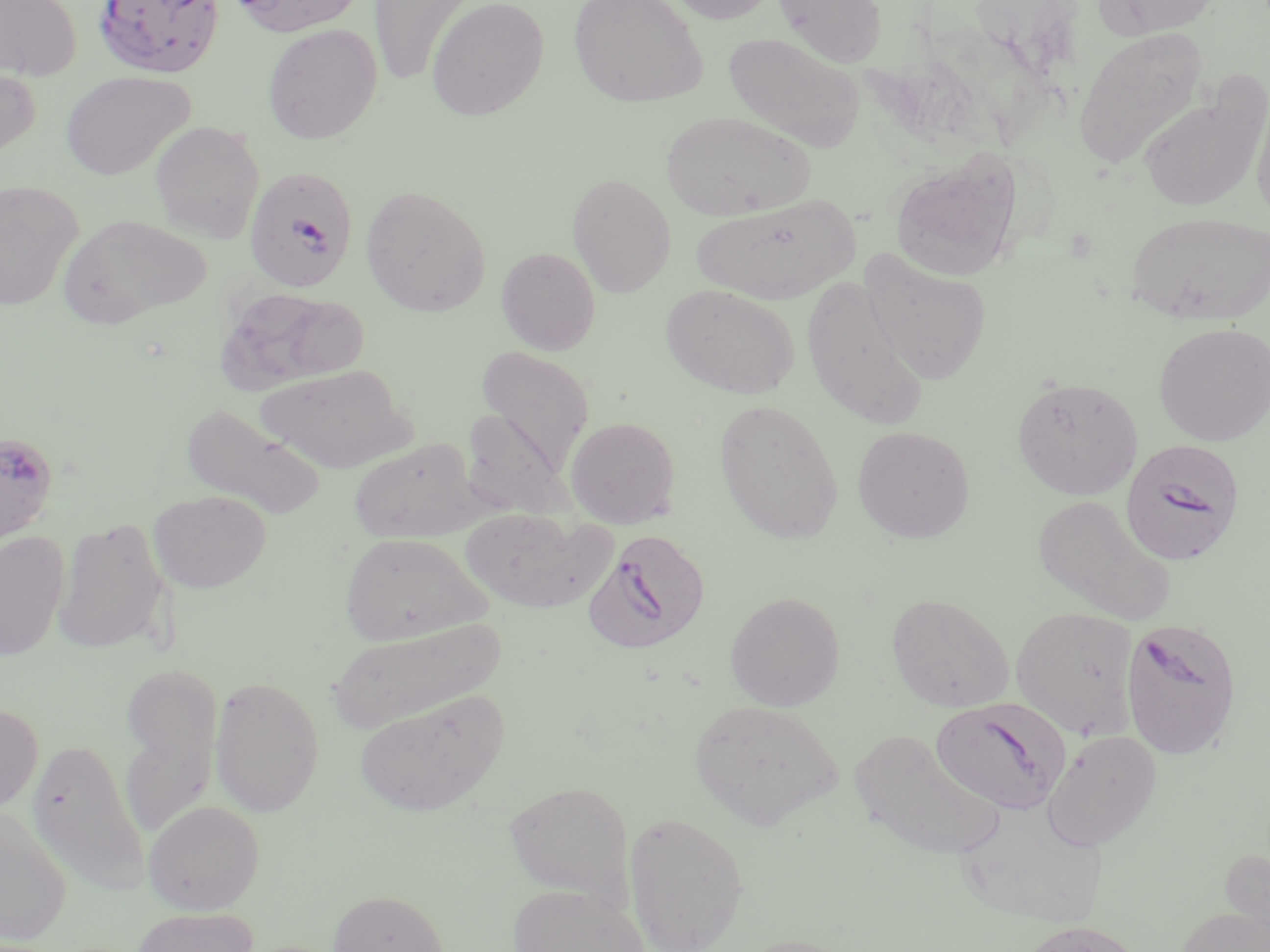
slide_level_diagnosis: Plasmodium falciparum
stain: May-Grünwald-Giemsa
image_size: 1270×952 pixels
modality: light microscopy
field_of_view: single
preparation: thin blood smear
uninfected_red_blood_cell_locations: 'approximate bounding boxes as (x1,y1)-(x2,y2) corner pairs in pixels: (0,0)-(81,81), (229,0)-(365,36), (426,0)-(549,121), (568,0)-(708,108), (664,0)-(781,24), (773,0)-(887,68), (1095,0)-(1220,38), (368,1)-(477,85), (262,23)-(382,143), (1072,27)-(1208,169), (724,31)-(865,152), (0,61)-(41,164), (61,70)-(195,180), (1137,82)-(1268,212), (1250,90)-(1270,225), (660,111)-(816,221), (150,121)-(265,242), (889,149)-(1023,282), (567,172)-(676,297), (0,180)-(84,310), (361,184)-(491,316), (689,194)-(861,305), (1125,211)-(1270,326), (59,213)-(210,328), (496,247)-(601,355), (859,250)-(992,386), (661,283)-(800,399), (220,288)-(369,391), (1153,322)-(1270,445), (475,346)-(594,476), (255,364)-(411,473), (1012,376)-(1143,499), (714,399)-(844,544), (181,404)-(326,519), (460,407)-(570,520), (565,417)-(681,528), (852,425)-(975,543), (350,438)-(479,543), (149,490)-(271,593), (1032,495)-(1177,625), (460,507)-(610,613), (54,516)-(170,656), (0,531)-(69,661), (339,532)-(490,646), (725,590)-(845,710), (886,593)-(1015,712), (1011,606)-(1139,740), (327,618)-(507,733), (120,664)-(221,832), (209,675)-(325,817), (354,690)-(508,818), (690,699)-(841,829), (0,702)-(43,817), (850,729)-(1005,860), (1042,729)-(1161,850), (27,737)-(149,895), (503,780)-(634,905), (143,800)-(264,914), (954,805)-(1107,930), (0,808)-(71,948), (623,811)-(749,951), (1220,849)-(1270,949), (506,883)-(650,952), (328,889)-(450,952), (1175,905)-(1270,952), (130,906)-(259,952), (1016,921)-(1145,952), (731,935)-(860,952)'
magnification: 1000x
plasmodium_falciparum_infected_red_blood_cell_locations: 'approximate bounding boxes as (x1,y1)-(x2,y2) corner pairs in pixels: (93,0)-(226,79), (243,172)-(356,298), (0,429)-(59,548), (1119,439)-(1245,566), (583,528)-(712,655), (1121,616)-(1243,759), (931,698)-(1069,814)'